Outline every malaria parasite.
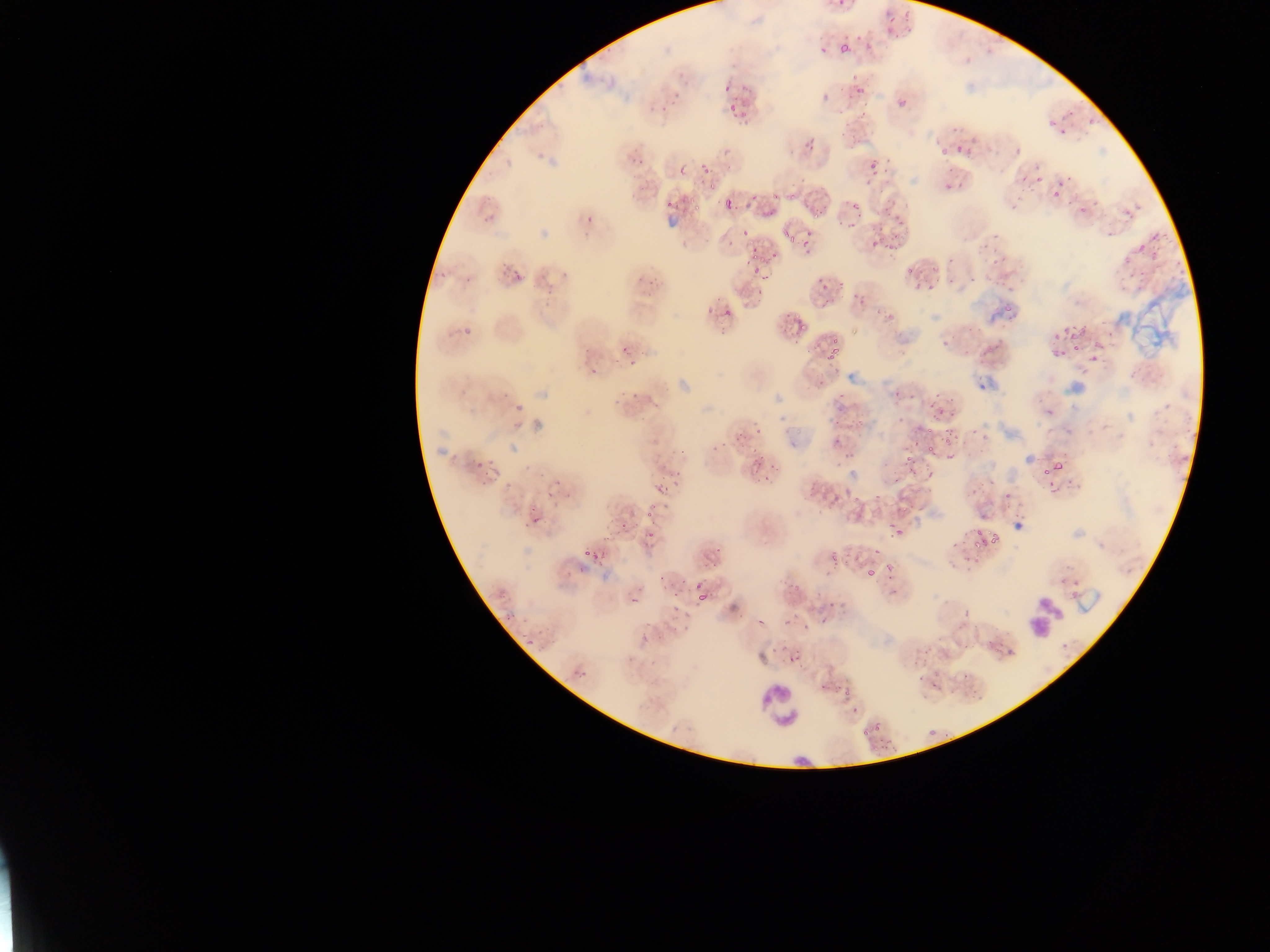

Approximate bounding boxes as {left, top, right, bottom} in pixels.
Malaria parasites: {882, 19, 901, 37}, {855, 30, 867, 47}, {816, 41, 830, 56}, {837, 44, 851, 62}, {737, 82, 750, 103}, {853, 83, 870, 97}, {668, 87, 689, 106}, {718, 87, 730, 99}, {816, 94, 835, 102}, {896, 97, 909, 111}, {725, 105, 736, 117}, {1085, 113, 1102, 131}, {1037, 121, 1064, 133}, {966, 130, 980, 147}, {1059, 133, 1070, 143}, {955, 139, 966, 151}, {802, 141, 821, 151}, {1008, 141, 1025, 158}, {932, 143, 950, 157}, {864, 157, 882, 176}, {694, 159, 716, 179}, {674, 162, 685, 176}, {1033, 162, 1045, 184}, {1020, 169, 1030, 183}, {859, 176, 871, 189}, {940, 177, 960, 193}, {1054, 179, 1067, 189}, {741, 187, 755, 216}, {1051, 192, 1060, 201}, {1088, 193, 1102, 206}, {1067, 194, 1090, 212}, {660, 196, 675, 209}, {886, 197, 898, 209}, {680, 198, 690, 219}, {723, 198, 733, 209}, {846, 203, 860, 214}, {807, 206, 824, 218}, {1120, 206, 1131, 217}, {480, 214, 493, 224}, {584, 214, 595, 226}, {889, 214, 907, 227}, {843, 218, 861, 232}, {736, 224, 749, 239}, {782, 229, 794, 240}, {800, 231, 815, 253}, {722, 234, 737, 256}, {889, 235, 903, 252}, {866, 239, 880, 250}, {979, 240, 996, 254}, {750, 241, 764, 254}, {1133, 243, 1150, 258}, {1139, 246, 1166, 263}, {500, 254, 513, 276}, {1117, 255, 1131, 273}, {905, 261, 919, 275}, {436, 262, 450, 281}, {751, 262, 766, 276}, {983, 267, 1001, 284}, {509, 269, 527, 285}, {464, 271, 475, 284}, {811, 273, 833, 298}, {635, 276, 656, 301}, {925, 280, 942, 294}, {538, 281, 556, 300}, {848, 290, 867, 303}, {780, 300, 798, 322}, {1002, 301, 1016, 312}, {723, 304, 734, 320}, {699, 308, 713, 322}, {875, 308, 894, 319}, {793, 318, 814, 340}, {461, 320, 474, 334}, {1054, 328, 1084, 342}, {818, 331, 840, 373}, {938, 336, 953, 354}, {618, 339, 634, 352}, {1046, 344, 1065, 366}, {1085, 349, 1103, 368}, {626, 360, 641, 371}, {584, 366, 600, 378}, {495, 388, 513, 402}, {924, 389, 943, 414}, {608, 391, 629, 409}, {509, 400, 527, 414}, {1040, 401, 1055, 415}, {946, 402, 963, 423}, {892, 409, 910, 427}, {969, 424, 982, 435}, {830, 425, 845, 446}, {733, 431, 745, 442}, {939, 432, 954, 455}, {915, 441, 941, 463}, {671, 444, 688, 458}, {1041, 448, 1077, 476}, {896, 450, 915, 479}, {749, 453, 758, 470}, {840, 453, 859, 461}, {473, 463, 484, 471}, {669, 463, 687, 478}, {765, 466, 781, 478}, {483, 467, 500, 484}, {762, 476, 778, 483}, {1003, 476, 1021, 503}, {662, 482, 673, 496}, {560, 486, 571, 502}, {543, 487, 557, 498}, {826, 491, 843, 511}, {850, 492, 865, 509}, {642, 508, 655, 522}, {524, 513, 537, 525}, {617, 519, 631, 538}, {884, 522, 906, 539}, {969, 524, 995, 550}, {644, 529, 654, 535}, {824, 548, 843, 567}, {579, 549, 593, 560}, {704, 553, 723, 567}, {862, 562, 878, 576}, {887, 564, 901, 583}, {563, 571, 574, 580}, {658, 573, 666, 586}, {679, 574, 693, 586}, {687, 590, 713, 612}, {661, 594, 678, 627}, {630, 596, 644, 610}, {503, 599, 521, 623}, {783, 608, 803, 627}, {516, 634, 536, 648}, {647, 644, 669, 670}, {787, 647, 803, 664}, {571, 669, 587, 687}, {822, 673, 832, 690}, {839, 683, 853, 702}, {854, 718, 880, 736}, {880, 731, 891, 755}.

Leukocyte locations: {1025, 594, 1065, 636}, {754, 681, 805, 734}. Sample from Ghana. Mobile-phone photograph taken through the microscope. Image is 1270×952 pixels. Single field of view. Thin blood film.